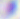

Summary:
  - Modality: photomicrograph
  - Magnification: 400x
  - Identification: Toxoplasma gondii